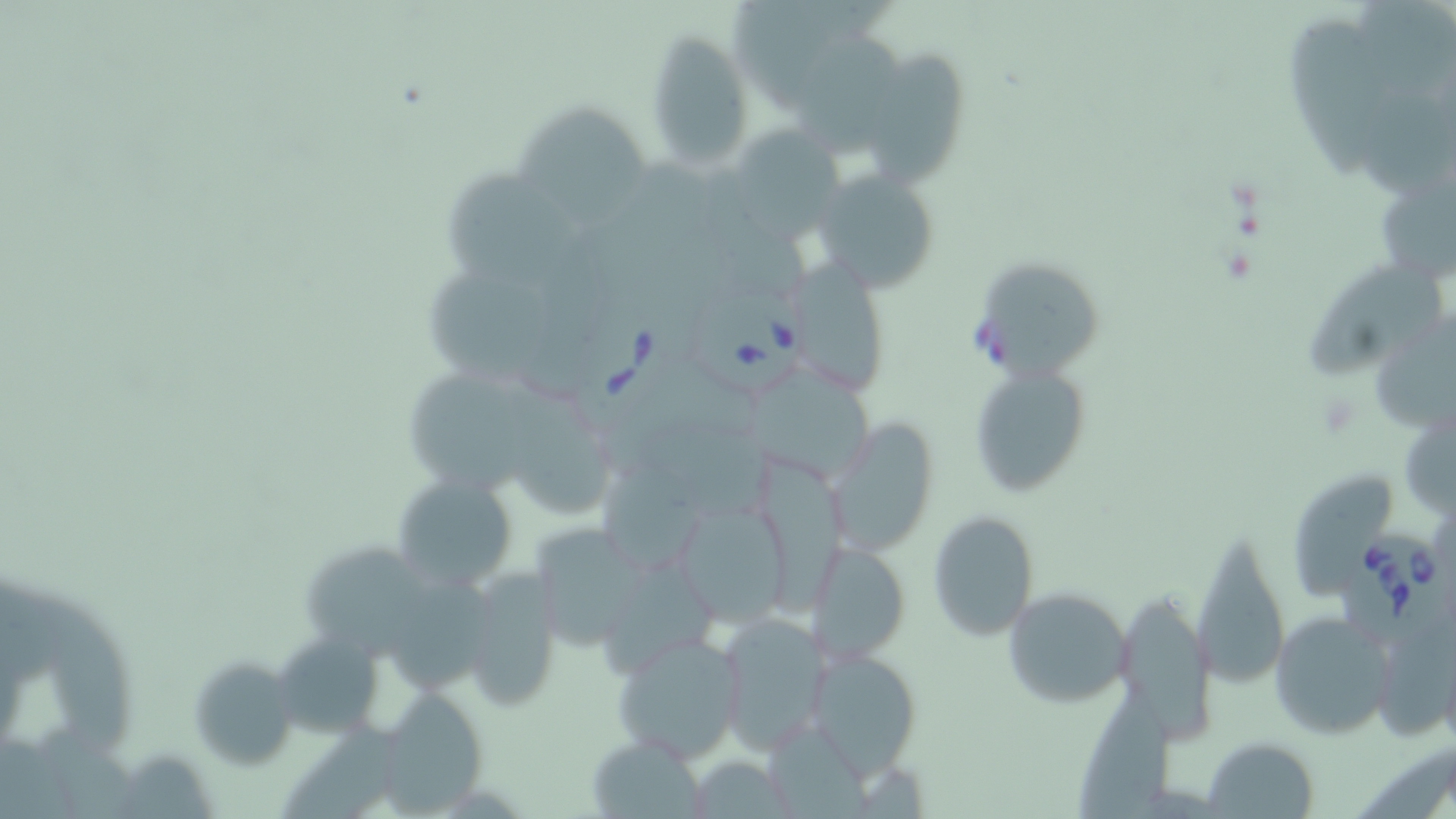

Summary:
  - Coordinate format: approximate bounding boxes as (x1, y1, x2, y2) in pixels
  - Uninfected red blood cell locations: (1359, 1, 1456, 95), (1285, 12, 1392, 185), (793, 30, 909, 155), (645, 32, 755, 173), (865, 51, 970, 199), (1354, 83, 1456, 193), (519, 107, 650, 232), (732, 125, 849, 243), (439, 165, 581, 298), (822, 174, 942, 292), (1309, 254, 1444, 383), (795, 263, 889, 400), (980, 264, 1102, 384), (428, 267, 560, 388), (967, 363, 1094, 499), (418, 370, 542, 493), (757, 371, 881, 490), (513, 390, 629, 518), (1398, 409, 1455, 523), (826, 419, 940, 559), (633, 423, 779, 523), (754, 452, 849, 622), (601, 461, 713, 572), (391, 471, 521, 591), (1292, 472, 1399, 605), (680, 497, 798, 638), (926, 509, 1041, 641), (538, 528, 653, 656), (1192, 529, 1292, 693), (808, 539, 910, 664), (462, 567, 564, 709), (1002, 587, 1134, 710), (1110, 595, 1216, 743), (27, 601, 135, 760), (1269, 611, 1395, 740), (715, 613, 832, 753), (612, 631, 747, 765), (271, 632, 386, 736), (807, 648, 922, 776), (189, 655, 299, 769), (373, 689, 489, 813), (281, 716, 404, 814), (585, 733, 708, 817), (1203, 736, 1320, 817)
  - Babesia divergens-infected red blood cell locations: (694, 292, 816, 391), (562, 300, 698, 437), (1338, 527, 1452, 640)
  - Slide-level diagnosis: Babesia divergens
  - Magnification: 1000x
  - Preparation: thin blood smear
  - Field of view: one of a larger specimen
  - Modality: optical microscopy
  - Image size: 1456×819 pixels
  - Stain: May-Grünwald-Giemsa